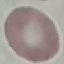

Malaria status: uninfected. Photographed with a smartphone camera at the microscope eyepiece. Giemsa-stained preparation. Cell patch, automatically extracted from a larger field of view and resized to 64 × 64 pixels. Thin smear of blood.